Identify the parasite.
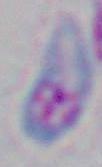

Toxoplasma gondii.

magnification: 1000x
modality: photomicrograph